Locate and identify every blood parasite.
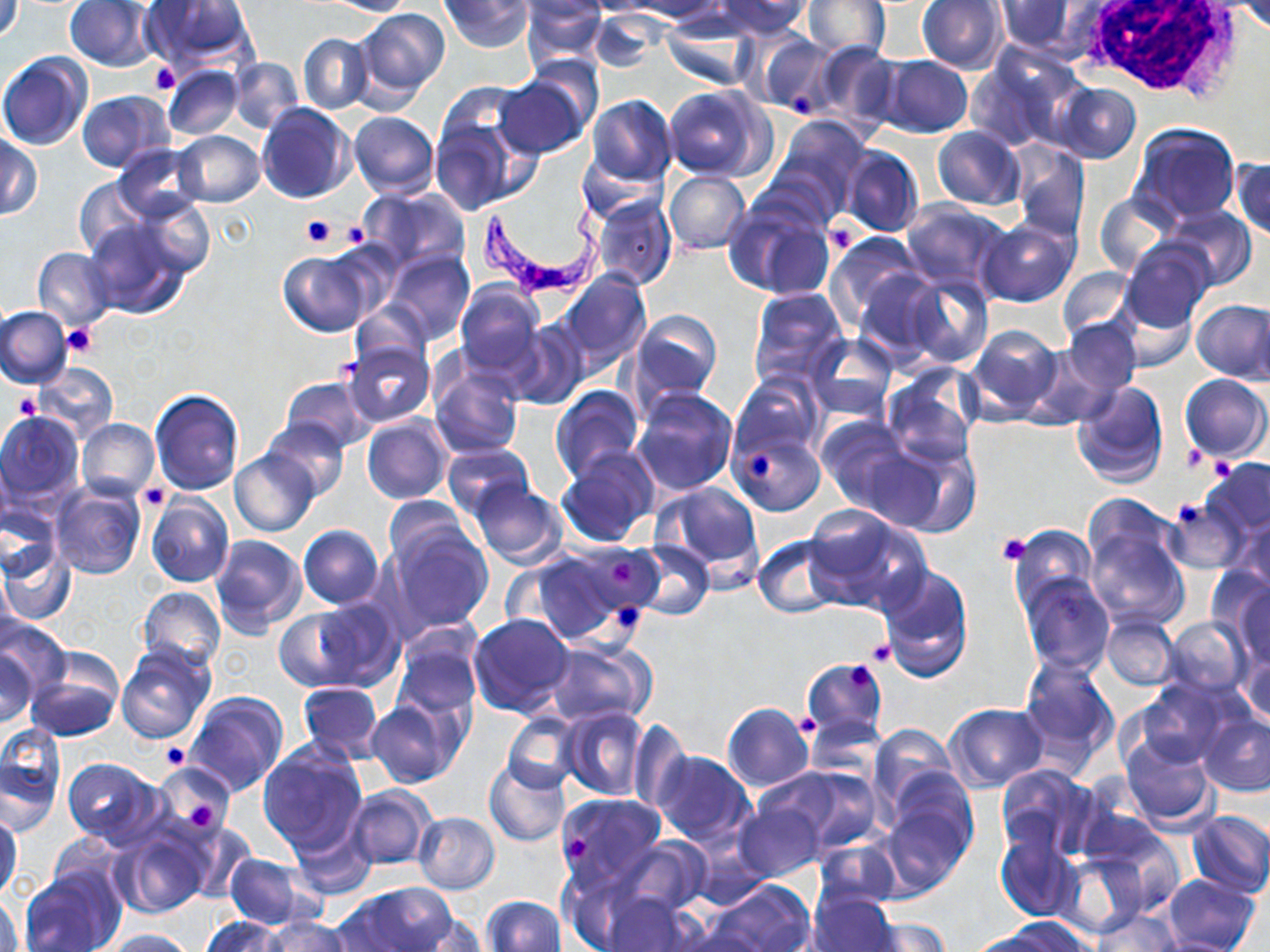

Approximate bounding boxes as (x1, y1, x2, y2) in pixels.
Trypanosoma brucei: (479, 187, 600, 296).
No Plasmodium falciparum, Plasmodium ovale, Plasmodium malariae, Plasmodium vivax, or Babesia divergens observed.

Summary:
  - Platelet locations: (149, 62, 179, 96), (790, 91, 815, 119), (300, 216, 336, 248), (335, 221, 370, 248), (824, 221, 862, 255), (62, 326, 97, 357), (13, 392, 40, 418), (1180, 445, 1207, 472), (750, 452, 774, 479), (1209, 453, 1238, 479), (138, 484, 168, 509), (1171, 497, 1214, 529), (994, 533, 1033, 565), (609, 560, 638, 586), (616, 603, 643, 628), (867, 640, 894, 665), (844, 662, 876, 689), (794, 715, 820, 739), (161, 741, 192, 770), (188, 802, 217, 828), (567, 833, 586, 860)
  - Uninfected red blood cell locations: (0, 0, 25, 44), (140, 0, 258, 73), (325, 0, 416, 16), (441, 0, 531, 51), (520, 0, 609, 72), (583, 0, 670, 16), (626, 0, 728, 21), (715, 0, 811, 38), (803, 0, 891, 61), (65, 1, 158, 71), (518, 1, 607, 27), (917, 1, 1007, 74), (996, 1, 1079, 55), (1232, 1, 1270, 32), (354, 7, 450, 103), (589, 11, 662, 75), (662, 19, 759, 90), (744, 28, 836, 116), (298, 33, 371, 114), (810, 42, 900, 131), (965, 48, 1079, 152), (0, 52, 92, 151), (879, 55, 973, 137), (228, 57, 305, 134), (162, 65, 242, 139), (495, 76, 588, 158), (1052, 81, 1141, 164), (666, 86, 770, 180), (77, 90, 173, 172), (585, 94, 678, 186), (428, 96, 530, 216), (256, 102, 354, 203), (348, 111, 439, 198), (768, 116, 872, 219), (1129, 122, 1241, 225), (932, 127, 1025, 210), (172, 131, 264, 208), (0, 133, 40, 220), (1011, 143, 1088, 241), (114, 144, 203, 219), (839, 146, 925, 239), (578, 151, 665, 224), (1232, 157, 1270, 241), (663, 171, 751, 255), (73, 177, 152, 260), (358, 185, 471, 274), (1093, 192, 1176, 277), (129, 194, 214, 280), (590, 194, 677, 290), (723, 196, 836, 299), (900, 200, 1014, 294), (1161, 206, 1257, 291), (82, 217, 190, 319), (975, 217, 1079, 307), (826, 231, 927, 325), (1121, 238, 1217, 337), (33, 247, 115, 330), (383, 249, 474, 345), (279, 250, 375, 335), (1057, 266, 1136, 342), (853, 267, 944, 366), (557, 270, 651, 368), (900, 272, 993, 369), (455, 280, 544, 375), (748, 286, 848, 387), (1124, 300, 1195, 372), (1192, 300, 1269, 383), (352, 302, 430, 370), (1250, 303, 1270, 389), (0, 305, 72, 389), (629, 309, 721, 404), (1060, 319, 1142, 397), (505, 320, 590, 410), (964, 323, 1063, 424), (805, 332, 899, 421), (1021, 335, 1122, 428), (343, 339, 436, 427), (32, 361, 117, 444), (429, 364, 525, 459), (884, 365, 981, 465), (732, 372, 823, 462), (1181, 374, 1268, 462), (281, 376, 373, 451), (1070, 381, 1169, 488), (550, 385, 644, 481), (150, 388, 244, 494), (631, 388, 738, 496), (0, 411, 84, 509), (362, 414, 452, 505), (816, 416, 910, 510), (262, 418, 350, 502), (76, 419, 160, 500), (731, 431, 824, 517), (866, 436, 980, 538), (443, 443, 531, 520), (555, 447, 661, 547), (230, 449, 319, 536), (1203, 458, 1270, 538), (1185, 479, 1265, 563), (468, 480, 567, 569), (51, 481, 146, 581), (654, 481, 761, 575), (146, 495, 234, 586), (383, 497, 472, 570), (1164, 497, 1245, 575), (0, 502, 61, 582), (804, 504, 928, 613), (1082, 506, 1191, 631), (1233, 510, 1270, 594), (385, 521, 493, 632), (297, 525, 383, 608), (1011, 525, 1095, 609), (210, 533, 307, 635), (753, 535, 845, 617), (631, 539, 715, 621), (1, 542, 76, 625), (519, 545, 643, 646), (876, 564, 974, 682), (1206, 565, 1270, 644), (1019, 571, 1114, 674), (0, 573, 22, 658), (1231, 577, 1270, 669), (137, 586, 227, 672), (313, 597, 405, 690), (274, 609, 360, 691), (469, 614, 574, 716), (1100, 615, 1179, 689), (1163, 616, 1250, 699), (0, 618, 72, 697), (391, 633, 480, 722), (543, 640, 655, 728), (116, 642, 216, 743), (1238, 647, 1269, 728), (0, 649, 38, 727), (25, 651, 124, 742), (1018, 656, 1118, 767), (800, 657, 887, 739), (1132, 680, 1240, 770), (296, 681, 384, 762), (186, 690, 288, 796), (366, 698, 462, 787), (722, 702, 813, 791), (943, 703, 1048, 791), (561, 706, 649, 801), (504, 712, 581, 793), (1198, 713, 1270, 796), (805, 714, 885, 778), (627, 720, 690, 810), (867, 723, 958, 816), (0, 727, 65, 831), (1120, 733, 1217, 831), (256, 741, 368, 857), (651, 751, 757, 846), (64, 757, 165, 849), (483, 757, 571, 847), (884, 761, 978, 861), (154, 763, 239, 839), (995, 763, 1099, 863), (759, 765, 881, 855), (345, 785, 435, 870), (555, 794, 667, 894), (877, 798, 974, 894), (734, 801, 825, 880), (1, 810, 22, 901), (1185, 811, 1270, 898), (413, 812, 499, 894), (289, 821, 377, 898), (112, 825, 212, 918), (1088, 826, 1185, 919), (993, 831, 1080, 921), (45, 833, 128, 904), (612, 836, 713, 919), (812, 837, 902, 912), (1053, 852, 1148, 937), (224, 853, 315, 928), (20, 870, 121, 951), (1161, 875, 1260, 952), (216, 876, 300, 951), (709, 879, 815, 952), (338, 883, 456, 951), (0, 889, 23, 952), (806, 892, 900, 952), (602, 893, 701, 952), (481, 895, 565, 952), (1092, 909, 1183, 952), (407, 913, 487, 952), (203, 915, 286, 952), (261, 915, 355, 952), (863, 916, 949, 952), (1001, 917, 1095, 952), (668, 926, 773, 952), (102, 929, 199, 951), (965, 930, 1054, 952), (1148, 935, 1250, 952)
  - White blood cell locations: (1073, 1, 1245, 102)
  - Slide-level diagnosis: Trypanosoma brucei
  - Modality: optical microscopy
  - Image size: 1270×952 pixels
  - Preparation: thin blood smear
  - Field of view: one of a larger specimen
  - Stain: May-Grünwald-Giemsa
  - Magnification: 1000x